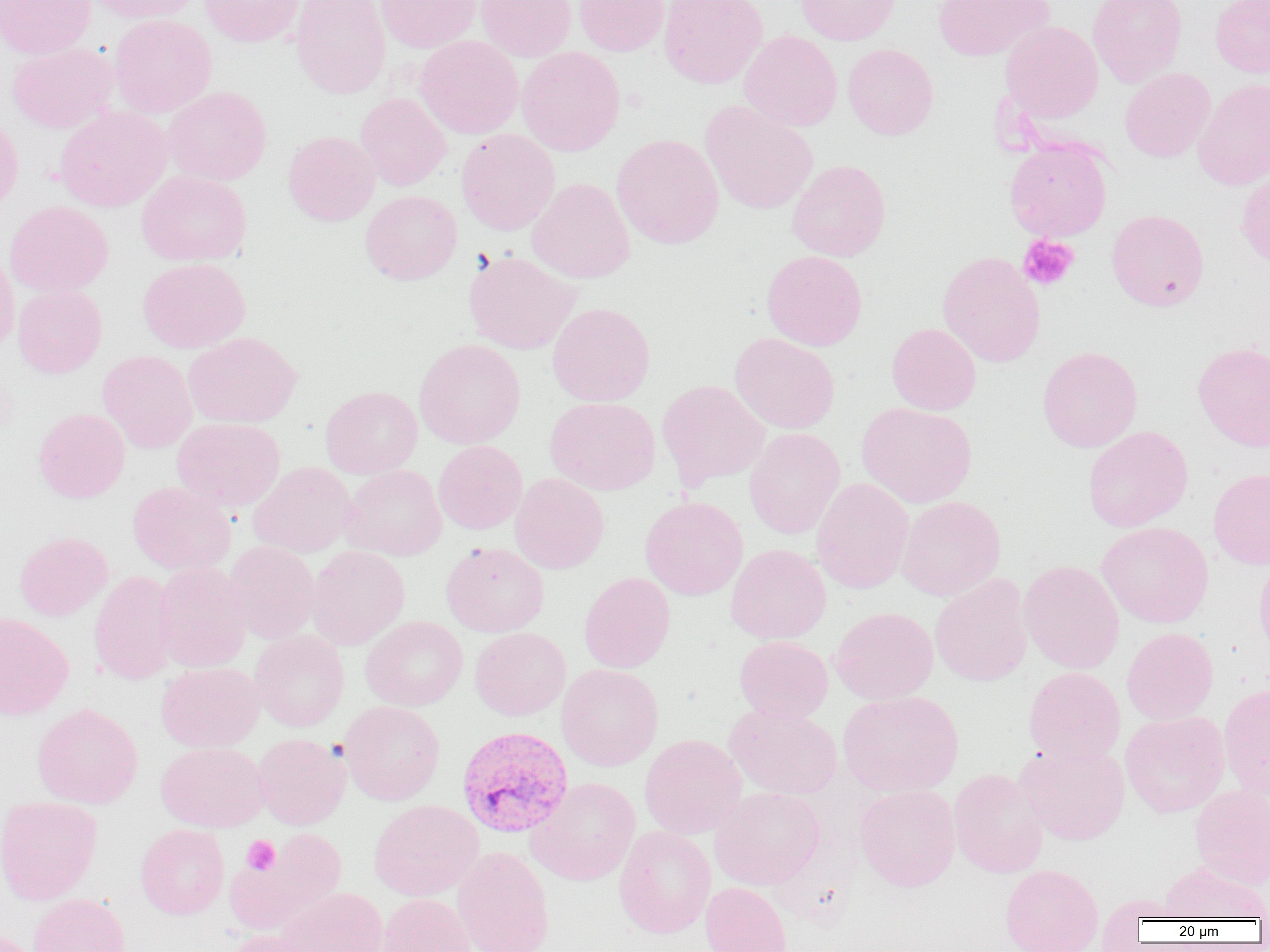
Summary:
  - Coordinate format: approximate bounding boxes as (x1,y1)-(x2,y2) corner pairs in pixels
  - Platelet locations: (1018,235)-(1079,291), (242,835)-(280,874)
  - Uninfected red blood cell locations: (0,0)-(96,59), (86,0)-(202,23), (199,0)-(304,47), (290,0)-(390,100), (375,0)-(481,53), (475,0)-(576,62), (574,0)-(669,56), (659,0)-(767,89), (795,0)-(900,45), (933,0)-(1052,61), (1087,0)-(1188,87), (1210,0)-(1270,78), (108,14)-(216,118), (1000,21)-(1103,123), (739,30)-(842,131), (415,35)-(523,139), (7,42)-(117,133), (843,43)-(938,140), (517,47)-(625,156), (1120,68)-(1216,162), (1193,78)-(1270,190), (163,86)-(272,186), (355,93)-(452,191), (700,101)-(818,215), (54,106)-(172,212), (0,114)-(23,215), (456,129)-(559,235), (282,131)-(380,226), (612,134)-(724,249), (1004,139)-(1112,241), (787,159)-(890,261), (1236,167)-(1270,268), (136,170)-(251,266), (527,178)-(634,284), (360,189)-(462,285), (4,201)-(113,297), (1106,209)-(1209,311), (0,250)-(19,356), (761,250)-(867,350), (464,251)-(581,355), (938,252)-(1045,367), (137,258)-(250,352), (12,285)-(107,378), (547,302)-(655,406), (886,323)-(981,415), (183,332)-(302,428), (730,333)-(839,434), (415,339)-(525,448), (1192,342)-(1270,451), (1037,346)-(1142,452), (98,350)-(197,453), (657,379)-(770,488), (321,386)-(422,478), (544,396)-(660,495), (857,402)-(977,508), (33,408)-(130,503), (172,417)-(285,512), (1083,426)-(1193,532), (744,428)-(845,539), (433,440)-(527,534), (248,462)-(356,557), (341,464)-(447,560), (1208,468)-(1270,570), (510,473)-(609,574), (812,478)-(914,594), (127,481)-(235,574), (640,496)-(748,600), (896,496)-(1006,601), (1097,522)-(1214,627), (14,532)-(112,621), (223,541)-(320,644), (441,542)-(549,637), (726,544)-(831,643), (306,546)-(409,650), (1254,552)-(1270,663), (1019,560)-(1124,674), (153,561)-(252,672), (89,571)-(179,685), (579,572)-(675,673), (930,574)-(1033,686), (830,607)-(938,704), (0,612)-(74,720), (360,615)-(468,711), (470,627)-(570,720), (1122,627)-(1218,724), (249,630)-(349,732), (734,636)-(833,723), (156,662)-(264,752), (556,664)-(664,771), (1023,667)-(1125,765), (1219,683)-(1270,802), (838,690)-(963,797), (339,701)-(444,805), (32,702)-(143,809), (724,704)-(842,800), (1120,710)-(1229,817), (252,733)-(350,830), (639,734)-(747,839), (1014,741)-(1130,845), (156,742)-(269,831), (949,769)-(1049,878), (526,777)-(641,886), (855,785)-(960,892), (1190,785)-(1270,889), (710,787)-(825,890), (0,796)-(102,905), (369,799)-(483,901), (135,824)-(229,919), (614,826)-(715,939), (226,829)-(346,935), (452,846)-(555,952), (1159,861)-(1269,922), (1000,864)-(1103,952), (700,882)-(793,952), (276,887)-(387,952), (29,893)-(130,952), (377,894)-(474,952), (0,928)-(42,952), (224,930)-(330,952)
  - Plasmodium vivax-infected red blood cell locations: (456,725)-(573,838)
  - Slide-level diagnosis: Plasmodium vivax
  - Image size: 1270×952 pixels
  - Modality: optical microscopy
  - Preparation: thin blood film
  - Magnification: 1000x
  - Field of view: single